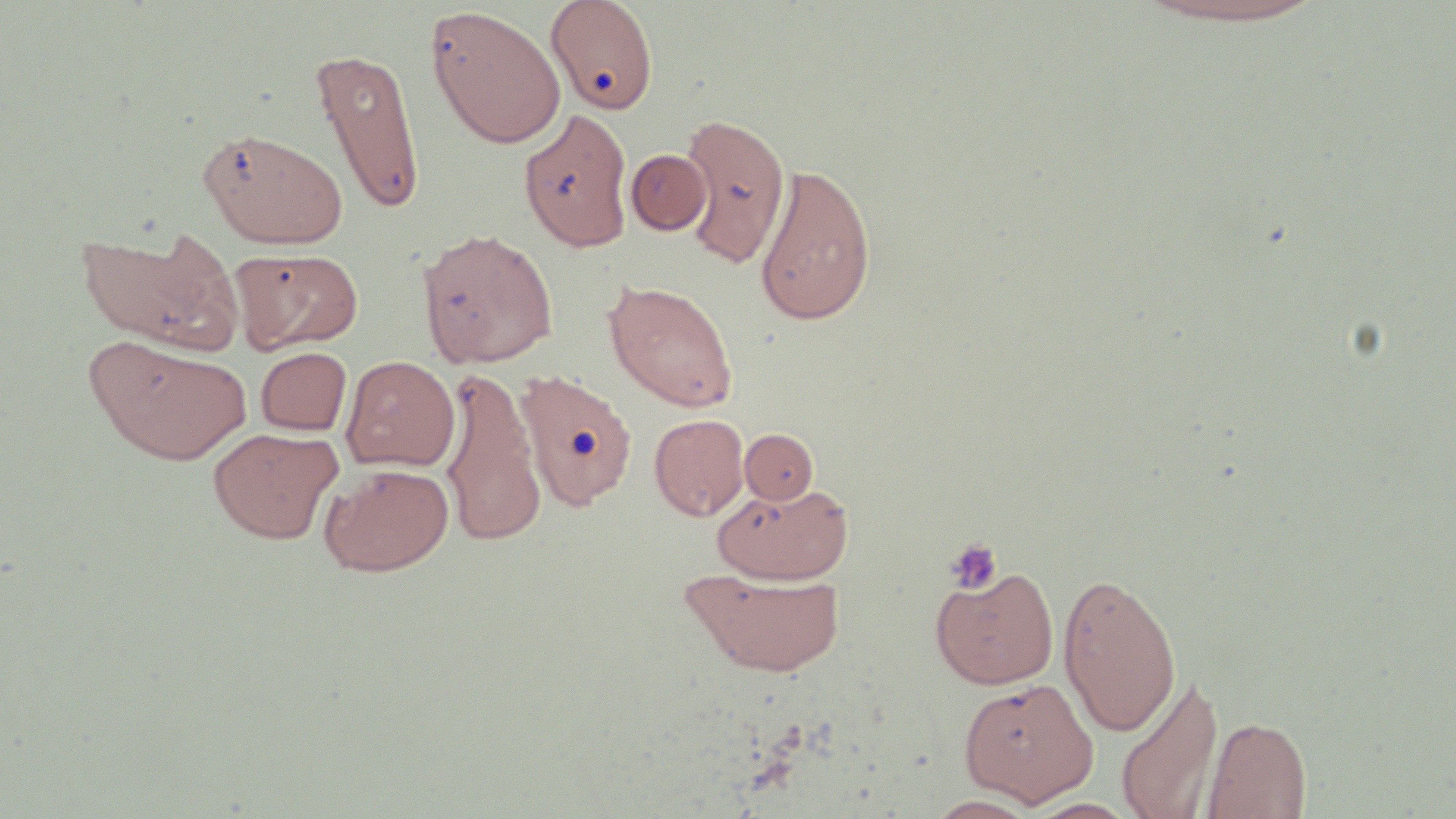

{
  "slide_level_diagnosis": "no evidence of blood parasites",
  "field_of_view": "single",
  "preparation": "thin blood smear",
  "modality": "light microscopy",
  "uninfected_red_blood_cell_locations": "approximate bounding boxes as [x1, y1, x2, y2] in pixels: [546, 0, 659, 114], [1136, 1, 1329, 28], [424, 6, 566, 149], [311, 47, 426, 215], [519, 107, 634, 252], [678, 112, 792, 270], [198, 126, 347, 249], [626, 148, 711, 235], [753, 162, 876, 326], [78, 225, 243, 355], [417, 227, 558, 368], [232, 247, 364, 353], [604, 279, 739, 413], [86, 335, 250, 465], [256, 347, 351, 435], [340, 355, 460, 471], [438, 366, 546, 548], [516, 369, 638, 511], [649, 413, 749, 520], [208, 427, 343, 544], [741, 428, 820, 505], [319, 462, 454, 576], [712, 481, 853, 583], [930, 565, 1059, 689], [683, 569, 846, 677], [1058, 570, 1182, 738], [1115, 673, 1223, 819], [960, 677, 1098, 806], [1202, 714, 1312, 818], [925, 794, 1042, 818]",
  "stain": "May-Grünwald-Giemsa",
  "platelet_locations": "approximate bounding boxes as [x1, y1, x2, y2] in pixels: [944, 537, 1003, 594]",
  "image_size": "1456×819 pixels",
  "magnification": "1000x"
}